Locate every malaria parasite.
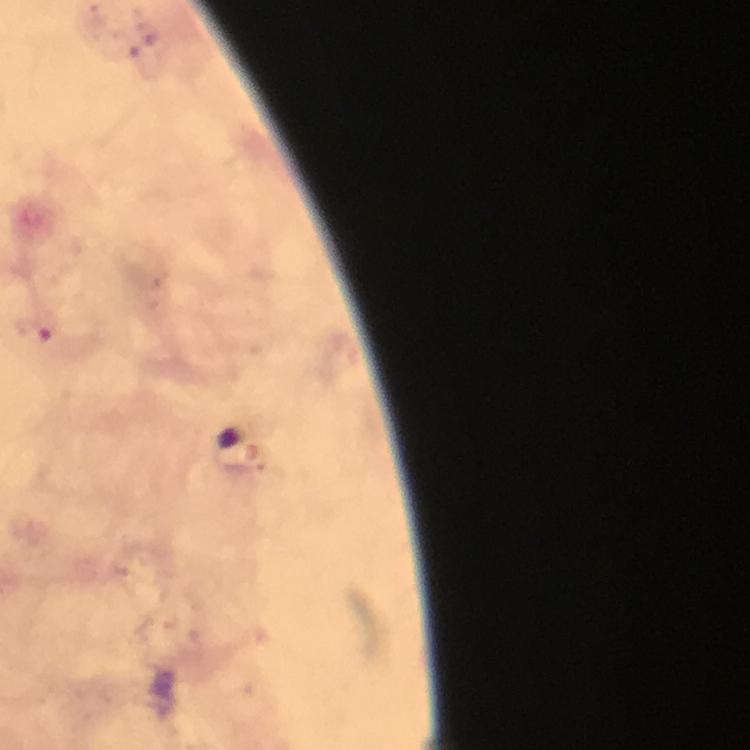
Approximate centers as {x, y} in pixels.
Malaria parasites: {38, 328}.

100x magnification. Photographed with a smartphone mounted on the microscope. Cropped region of a single field of view. From a diagnostic examination for malaria. Giemsa-stained preparation. Image is 750×750 pixels. Immersion oil applied. Thick blood film.